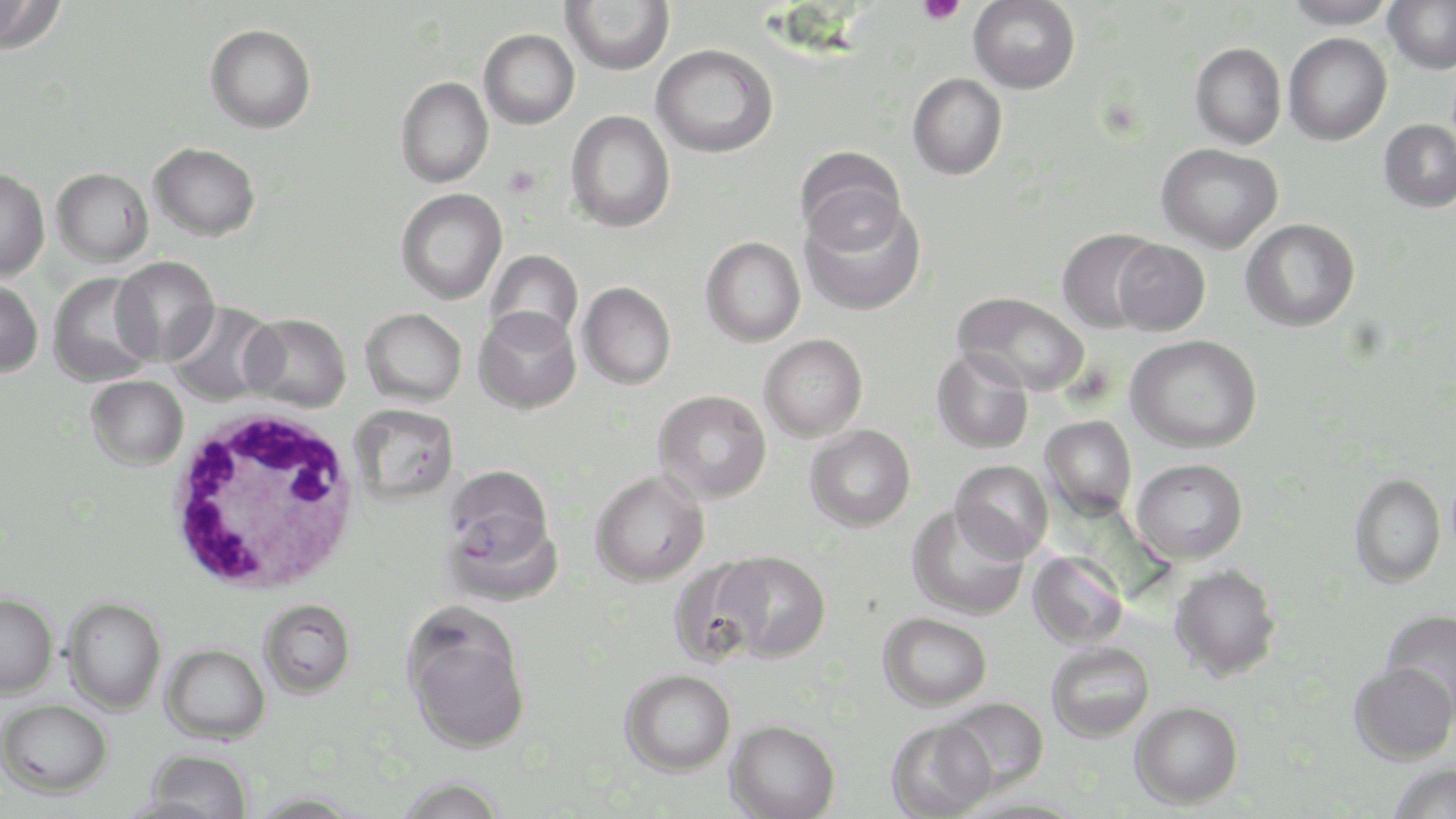
{
  "slide_level_diagnosis": "Plasmodium falciparum",
  "image_size": "1456×819 pixels",
  "field_of_view": "one of a larger specimen",
  "stain": "May-Grünwald-Giemsa",
  "platelet_locations": "approximate bounding boxes as [x1, y1, x2, y2] in pixels: [916, 0, 965, 26], [504, 165, 541, 199]",
  "white_blood_cell_locations": "approximate bounding boxes as [x1, y1, x2, y2] in pixels: [165, 405, 360, 594]",
  "magnification": "1000x",
  "uninfected_red_blood_cell_locations": "approximate bounding boxes as [x1, y1, x2, y2] in pixels: [0, 0, 66, 54], [561, 0, 675, 75], [969, 0, 1081, 94], [1283, 0, 1398, 29], [1382, 0, 1456, 74], [205, 23, 317, 133], [478, 28, 580, 129], [1283, 33, 1392, 145], [1190, 42, 1287, 150], [651, 44, 778, 158], [907, 73, 1008, 180], [396, 76, 494, 188], [566, 109, 675, 233], [1378, 119, 1456, 212], [149, 142, 261, 241], [1156, 143, 1283, 253], [795, 145, 907, 251], [0, 167, 50, 280], [52, 167, 153, 267], [395, 188, 507, 305], [799, 197, 926, 317], [1241, 218, 1361, 332], [1057, 228, 1162, 334], [700, 236, 806, 347], [1112, 239, 1211, 336], [484, 249, 583, 347], [110, 256, 219, 365], [47, 273, 157, 387], [0, 279, 44, 376], [577, 281, 676, 389], [953, 292, 1090, 396], [165, 301, 280, 406], [361, 307, 467, 407], [473, 307, 581, 415], [242, 313, 352, 412], [759, 334, 868, 442], [1126, 334, 1262, 454], [932, 347, 1035, 454], [86, 374, 189, 469], [653, 390, 771, 503], [348, 403, 460, 505], [1041, 415, 1138, 517], [805, 425, 916, 532], [1131, 458, 1248, 564], [950, 459, 1054, 562], [591, 470, 710, 587], [1349, 472, 1447, 589], [908, 505, 1031, 620], [444, 509, 563, 607], [713, 550, 831, 661], [1028, 551, 1128, 649], [667, 557, 770, 667], [1169, 563, 1282, 681], [0, 593, 58, 698], [64, 596, 166, 714], [258, 599, 355, 698], [1380, 608, 1456, 719], [878, 612, 992, 710], [405, 615, 531, 753], [1046, 641, 1155, 742], [161, 643, 270, 743], [1349, 662, 1455, 764], [619, 668, 736, 775], [945, 697, 1050, 793], [1, 698, 112, 798], [1130, 701, 1244, 809], [725, 719, 840, 819], [885, 719, 996, 819], [145, 748, 253, 819], [1387, 763, 1456, 819], [396, 775, 507, 819]",
  "preparation": "thin blood film",
  "plasmodium_falciparum_infected_red_blood_cell_locations": "approximate bounding boxes as [x1, y1, x2, y2] in pixels: [445, 465, 553, 559]",
  "modality": "optical microscopy"
}